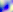
{
  "magnification": "400x",
  "modality": "micrograph",
  "identification": "Toxoplasma gondii"
}